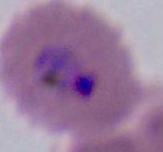

Photomicrograph. Captured at either 400x or 1000x magnification. A Plasmodium parasite is shown.